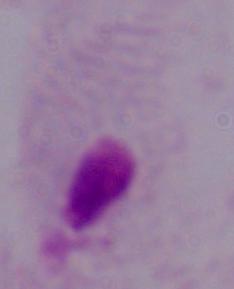

magnification = 1000x
identification = trichomonad
modality = photomicrograph